Describe the morphology of the red blood cells.
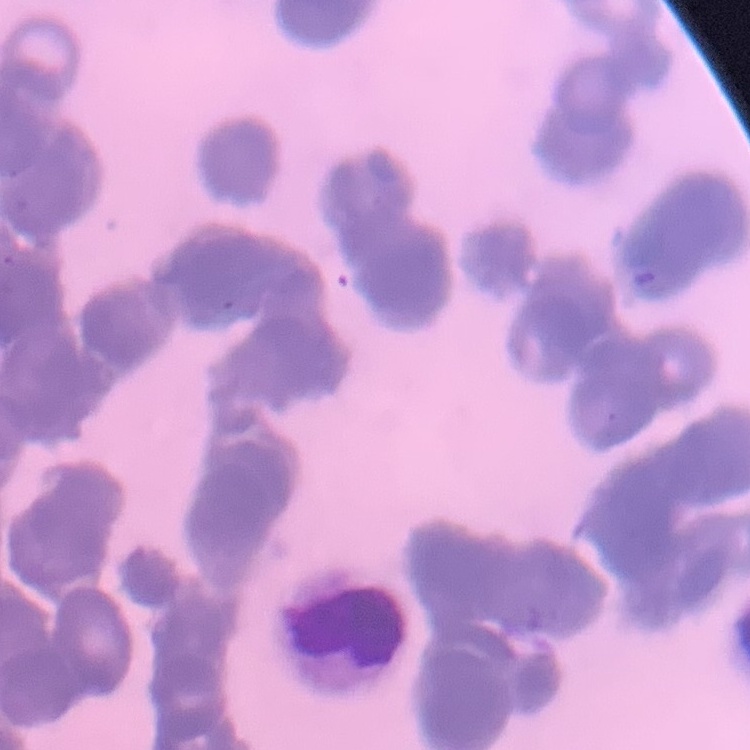

They show rouleaux formation.

One tile cut from a larger photomicrograph. Stained with either Field's or Giemsa. Thin blood film.